Outline every artifact (platelet-like body, stain precipitate, or debris).
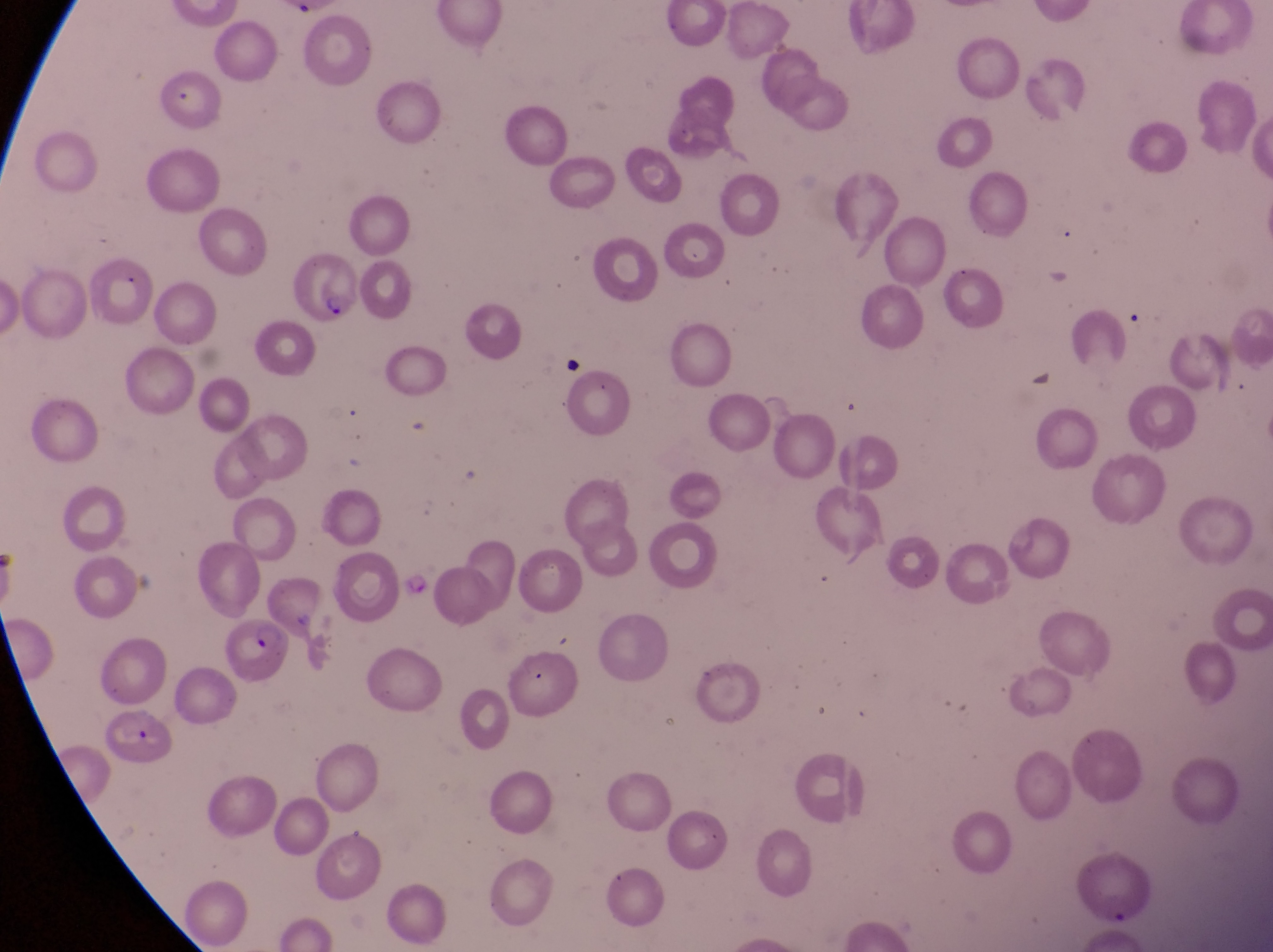
Approximate bounding boxes as {left, top, right, bottom} in pixels.
Artifacts (platelet-like body, stain precipitate, or debris): {556, 347, 599, 386}.

Parasitised red blood cell locations: {290, 252, 364, 327}, {220, 612, 295, 689}. Sample from Uganda. Captured by a smartphone held over the eyepiece of an Olympus CX-23 microscope. At a magnification of 1000x. Image is 1273×952 pixels. Thin blood film. One field of view.